Locate platelets.
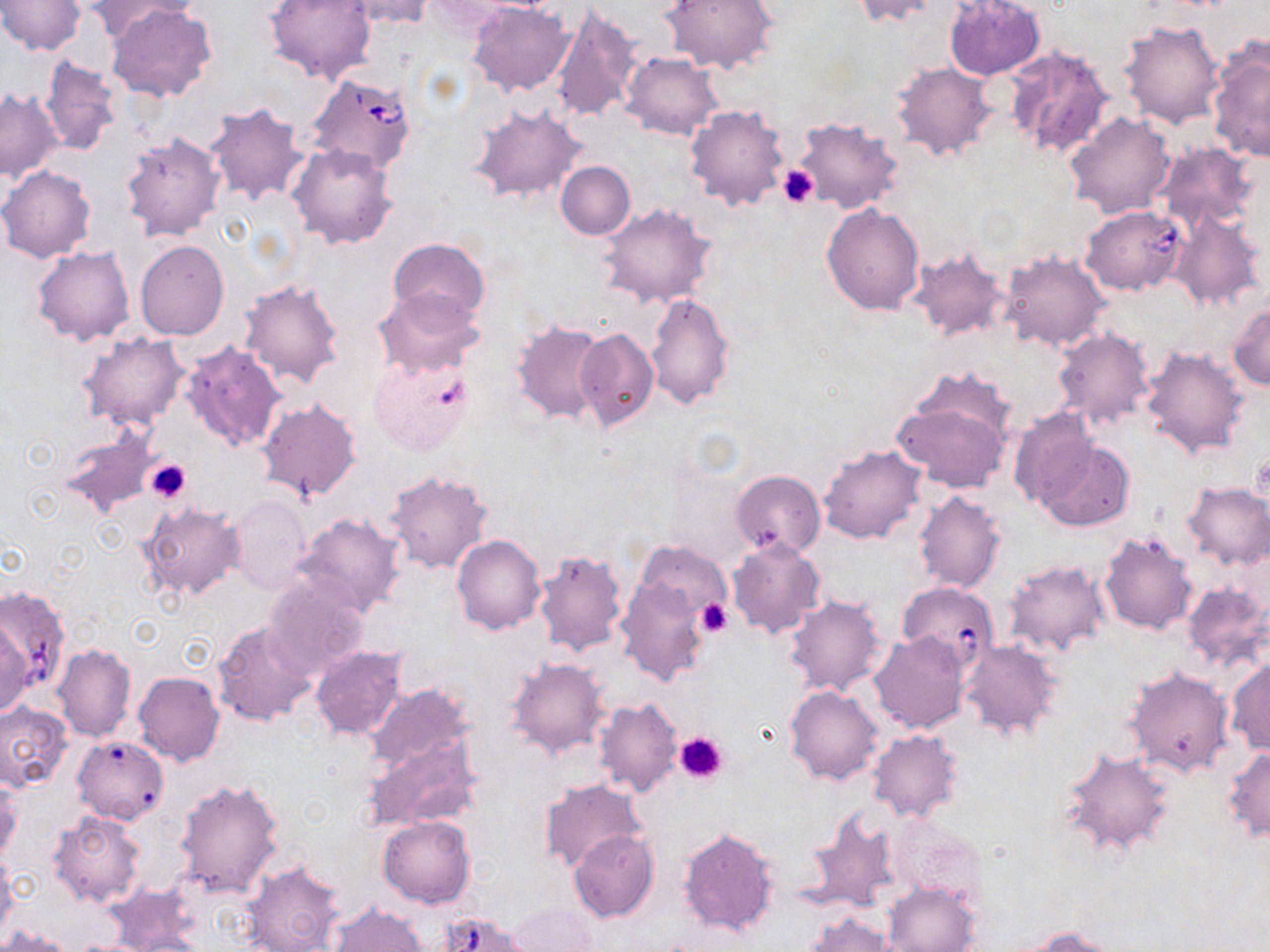

Approximate bounding boxes as named x1/y1/x2/y2 corners in pixels.
Platelets: (x1=778, y1=164, x2=818, y2=208), (x1=1250, y1=453, x2=1268, y2=501), (x1=144, y1=459, x2=192, y2=502), (x1=694, y1=597, x2=733, y2=638), (x1=674, y1=730, x2=728, y2=785).

Uninfected red blood cell locations: (x1=1, y1=0, x2=84, y2=55), (x1=86, y1=0, x2=195, y2=41), (x1=264, y1=0, x2=375, y2=85), (x1=340, y1=0, x2=436, y2=28), (x1=661, y1=0, x2=777, y2=75), (x1=850, y1=0, x2=945, y2=25), (x1=943, y1=0, x2=1044, y2=81), (x1=468, y1=2, x2=574, y2=97), (x1=108, y1=4, x2=216, y2=103), (x1=551, y1=7, x2=639, y2=122), (x1=1119, y1=20, x2=1224, y2=128), (x1=1207, y1=41, x2=1270, y2=163), (x1=1004, y1=44, x2=1115, y2=159), (x1=623, y1=53, x2=723, y2=139), (x1=39, y1=55, x2=121, y2=156), (x1=891, y1=60, x2=998, y2=161), (x1=1, y1=88, x2=62, y2=180), (x1=204, y1=102, x2=310, y2=207), (x1=685, y1=103, x2=789, y2=210), (x1=468, y1=105, x2=587, y2=202), (x1=1064, y1=111, x2=1177, y2=219), (x1=792, y1=116, x2=905, y2=214), (x1=120, y1=132, x2=227, y2=242), (x1=286, y1=143, x2=398, y2=249), (x1=1151, y1=143, x2=1258, y2=234), (x1=556, y1=161, x2=635, y2=239), (x1=0, y1=167, x2=96, y2=262), (x1=821, y1=202, x2=925, y2=314), (x1=598, y1=203, x2=717, y2=308), (x1=1167, y1=209, x2=1265, y2=313), (x1=388, y1=238, x2=491, y2=325), (x1=136, y1=241, x2=229, y2=340), (x1=32, y1=246, x2=135, y2=346), (x1=908, y1=247, x2=1011, y2=342), (x1=999, y1=249, x2=1109, y2=352), (x1=239, y1=278, x2=346, y2=389), (x1=373, y1=288, x2=486, y2=378), (x1=645, y1=292, x2=735, y2=411), (x1=1229, y1=301, x2=1270, y2=391), (x1=510, y1=319, x2=608, y2=425), (x1=1051, y1=326, x2=1155, y2=430), (x1=575, y1=327, x2=659, y2=432), (x1=78, y1=332, x2=189, y2=430), (x1=180, y1=343, x2=287, y2=453), (x1=1140, y1=345, x2=1251, y2=459), (x1=367, y1=353, x2=476, y2=455), (x1=891, y1=383, x2=1012, y2=492), (x1=256, y1=399, x2=363, y2=503), (x1=1007, y1=407, x2=1097, y2=514), (x1=58, y1=430, x2=158, y2=519), (x1=1037, y1=440, x2=1133, y2=532), (x1=819, y1=444, x2=927, y2=544), (x1=383, y1=468, x2=493, y2=574), (x1=731, y1=469, x2=825, y2=559), (x1=1180, y1=481, x2=1269, y2=571), (x1=914, y1=492, x2=1007, y2=594), (x1=229, y1=494, x2=313, y2=593), (x1=138, y1=501, x2=245, y2=602), (x1=293, y1=512, x2=407, y2=619), (x1=1100, y1=529, x2=1199, y2=635), (x1=452, y1=533, x2=545, y2=635), (x1=727, y1=537, x2=824, y2=637), (x1=637, y1=542, x2=730, y2=622), (x1=532, y1=548, x2=628, y2=656), (x1=1003, y1=559, x2=1111, y2=659), (x1=261, y1=573, x2=368, y2=681), (x1=614, y1=574, x2=709, y2=686), (x1=1181, y1=581, x2=1269, y2=674), (x1=784, y1=595, x2=885, y2=697), (x1=211, y1=619, x2=318, y2=727), (x1=0, y1=621, x2=32, y2=716), (x1=869, y1=632, x2=971, y2=734), (x1=958, y1=638, x2=1062, y2=742), (x1=53, y1=644, x2=136, y2=742), (x1=310, y1=645, x2=406, y2=741), (x1=504, y1=656, x2=611, y2=760), (x1=1226, y1=659, x2=1270, y2=755), (x1=1125, y1=667, x2=1233, y2=777), (x1=133, y1=671, x2=224, y2=766), (x1=364, y1=683, x2=474, y2=774), (x1=785, y1=685, x2=883, y2=785), (x1=593, y1=697, x2=683, y2=799), (x1=0, y1=702, x2=71, y2=790), (x1=867, y1=729, x2=963, y2=823), (x1=361, y1=732, x2=483, y2=833), (x1=72, y1=736, x2=169, y2=825), (x1=1058, y1=746, x2=1178, y2=860), (x1=1223, y1=746, x2=1270, y2=843), (x1=0, y1=777, x2=21, y2=865), (x1=172, y1=777, x2=284, y2=898), (x1=539, y1=779, x2=647, y2=873), (x1=800, y1=808, x2=904, y2=915), (x1=49, y1=812, x2=145, y2=908), (x1=378, y1=815, x2=475, y2=908), (x1=890, y1=815, x2=987, y2=905), (x1=676, y1=825, x2=779, y2=938), (x1=569, y1=829, x2=659, y2=922), (x1=0, y1=856, x2=17, y2=944), (x1=242, y1=859, x2=345, y2=952), (x1=882, y1=882, x2=979, y2=951), (x1=507, y1=902, x2=598, y2=952), (x1=328, y1=904, x2=428, y2=951), (x1=805, y1=913, x2=897, y2=952), (x1=1017, y1=925, x2=1122, y2=951), (x1=1, y1=927, x2=73, y2=952). Babesia divergens-infected red blood cell locations: (x1=305, y1=73, x2=418, y2=178), (x1=1082, y1=205, x2=1187, y2=294), (x1=1, y1=586, x2=69, y2=695). Slide-level diagnosis: Babesia divergens. May-Grünwald-Giemsa-stained preparation. Image is 1270×952 pixels. Single field of view. 1000x magnification. Thin blood smear. Light microscopy.